State the preparation type.
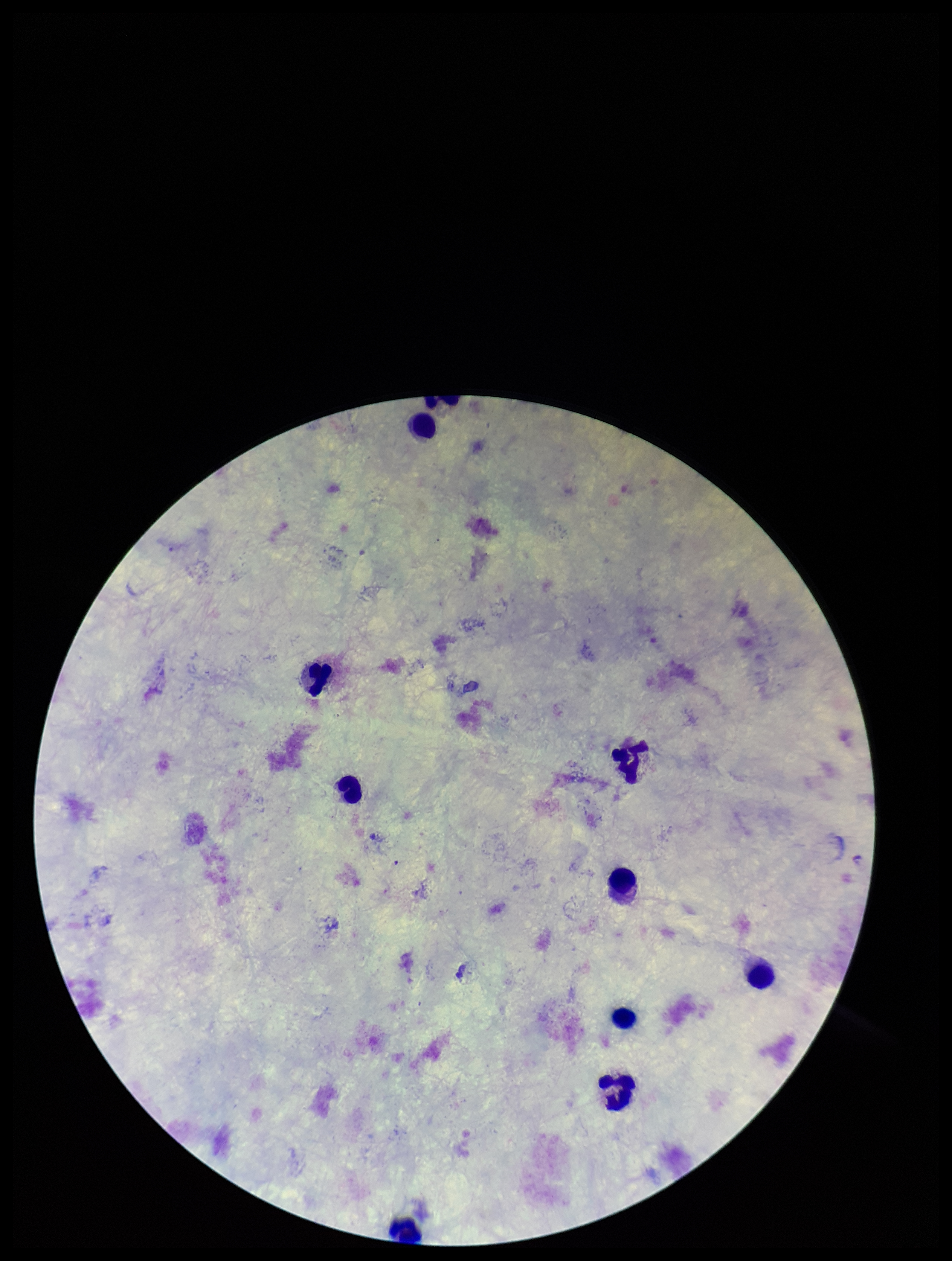

It is a thick blood smear.

Leukocyte count: 9. Giemsa stain. Photographed through the microscope eyepiece with a smartphone camera. Parasite count: 0. Plasmodium parasites: none seen. Patient malaria status: negative. Image is 952×1261 pixels. Single field of view.